Mark where platelets are.
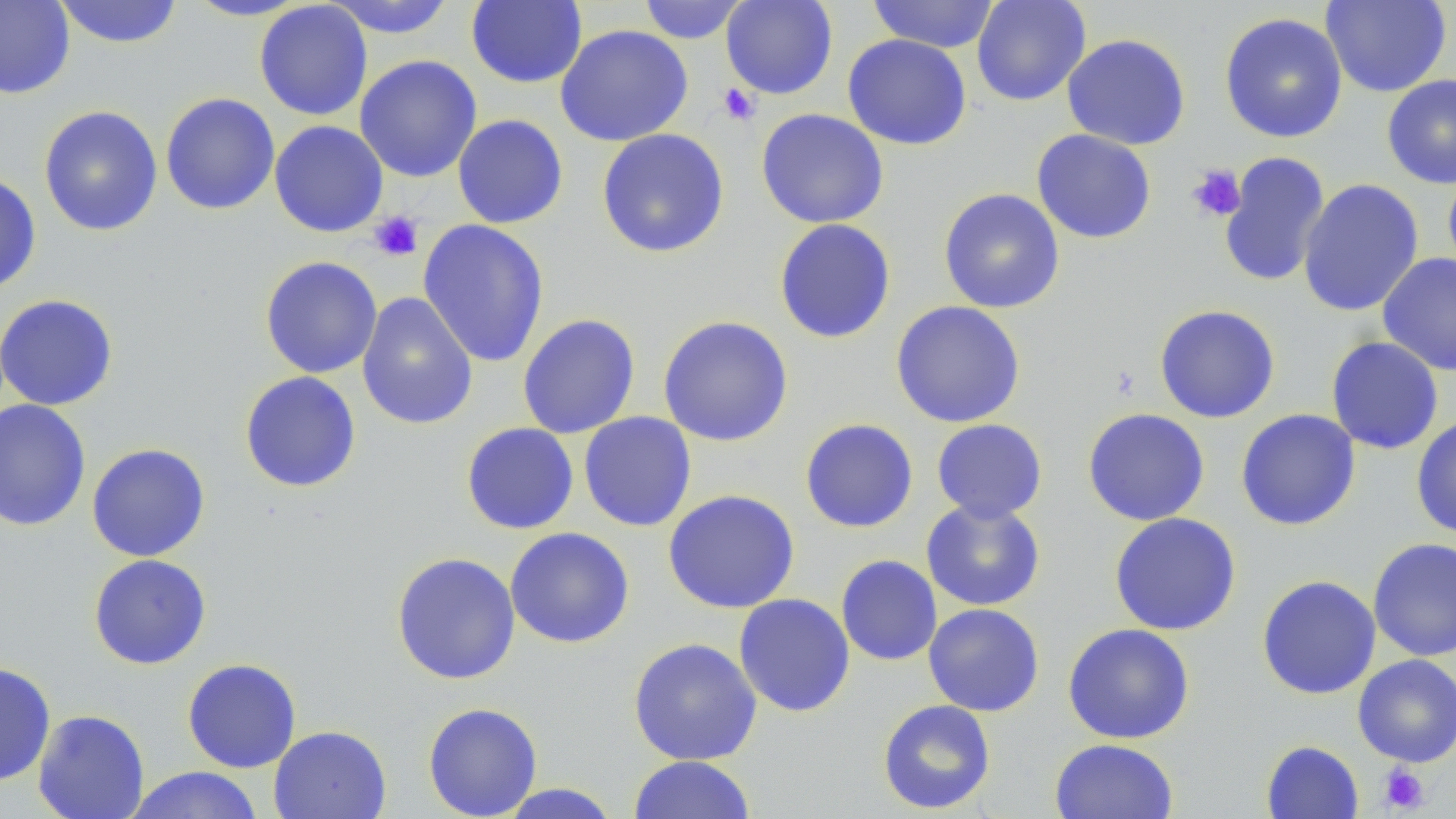
Approximate bounding boxes as named x1/y1/x2/y2 corners in pixels.
Platelets: (x1=717, y1=83, x2=760, y2=126), (x1=1188, y1=164, x2=1247, y2=222), (x1=369, y1=211, x2=424, y2=261), (x1=1378, y1=763, x2=1430, y2=814).

slide_level_diagnosis: negative for blood parasites
magnification: 1000x
modality: optical microscopy
uninfected_red_blood_cell_locations: 'approximate bounding boxes as named x1/y1/x2/y2 corners in pixels: (x1=0, y1=0, x2=75, y2=99), (x1=52, y1=0, x2=184, y2=49), (x1=182, y1=0, x2=312, y2=21), (x1=321, y1=0, x2=458, y2=39), (x1=637, y1=0, x2=750, y2=44), (x1=720, y1=0, x2=838, y2=100), (x1=867, y1=0, x2=1000, y2=53), (x1=971, y1=0, x2=1091, y2=106), (x1=1321, y1=0, x2=1452, y2=97), (x1=254, y1=1, x2=373, y2=121), (x1=466, y1=1, x2=588, y2=89), (x1=1219, y1=12, x2=1348, y2=143), (x1=554, y1=24, x2=693, y2=147), (x1=1061, y1=33, x2=1191, y2=150), (x1=842, y1=34, x2=972, y2=151), (x1=354, y1=54, x2=482, y2=182), (x1=1381, y1=74, x2=1456, y2=189), (x1=160, y1=92, x2=280, y2=215), (x1=38, y1=104, x2=163, y2=237), (x1=756, y1=108, x2=889, y2=229), (x1=452, y1=114, x2=569, y2=229), (x1=269, y1=120, x2=389, y2=238), (x1=597, y1=128, x2=730, y2=258), (x1=1031, y1=129, x2=1157, y2=244), (x1=1218, y1=151, x2=1331, y2=289), (x1=1442, y1=168, x2=1456, y2=283), (x1=0, y1=173, x2=41, y2=294), (x1=1298, y1=178, x2=1424, y2=317), (x1=938, y1=187, x2=1066, y2=314), (x1=773, y1=218, x2=897, y2=344), (x1=418, y1=219, x2=550, y2=368), (x1=1377, y1=253, x2=1456, y2=376), (x1=259, y1=256, x2=383, y2=379), (x1=356, y1=291, x2=479, y2=430), (x1=0, y1=294, x2=118, y2=411), (x1=890, y1=300, x2=1027, y2=428), (x1=1154, y1=304, x2=1281, y2=423), (x1=517, y1=314, x2=640, y2=439), (x1=657, y1=315, x2=794, y2=447), (x1=1325, y1=336, x2=1444, y2=454), (x1=239, y1=371, x2=362, y2=493), (x1=0, y1=399, x2=92, y2=532), (x1=1082, y1=407, x2=1210, y2=526), (x1=1235, y1=408, x2=1362, y2=531), (x1=578, y1=411, x2=697, y2=532), (x1=1411, y1=416, x2=1456, y2=540), (x1=799, y1=418, x2=919, y2=533), (x1=931, y1=419, x2=1048, y2=523), (x1=460, y1=422, x2=579, y2=535), (x1=86, y1=443, x2=211, y2=562), (x1=662, y1=489, x2=801, y2=614), (x1=920, y1=498, x2=1046, y2=611), (x1=1108, y1=512, x2=1241, y2=636), (x1=505, y1=527, x2=635, y2=649), (x1=1367, y1=537, x2=1456, y2=661), (x1=391, y1=552, x2=521, y2=685), (x1=88, y1=553, x2=212, y2=670), (x1=835, y1=554, x2=943, y2=666), (x1=1256, y1=575, x2=1382, y2=700), (x1=733, y1=593, x2=855, y2=717), (x1=922, y1=603, x2=1045, y2=717), (x1=1063, y1=623, x2=1195, y2=744), (x1=628, y1=637, x2=762, y2=766), (x1=1353, y1=654, x2=1456, y2=767), (x1=182, y1=658, x2=302, y2=773), (x1=0, y1=661, x2=56, y2=787), (x1=877, y1=699, x2=997, y2=814), (x1=422, y1=702, x2=543, y2=818), (x1=32, y1=709, x2=150, y2=819), (x1=269, y1=725, x2=392, y2=819), (x1=1049, y1=738, x2=1179, y2=819), (x1=1261, y1=740, x2=1364, y2=818), (x1=629, y1=756, x2=756, y2=818), (x1=123, y1=766, x2=265, y2=819), (x1=496, y1=783, x2=622, y2=818)'
preparation: thin blood smear
image_size: 1456×819 pixels
stain: May-Grünwald-Giemsa
field_of_view: single